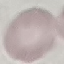
malaria_status: uninfected
image_type: cell patch, automatically extracted from a larger field of view and resized to 64 × 64 pixels
stain: Giemsa
capture: smartphone camera at the microscope eyepiece
preparation: thin blood film